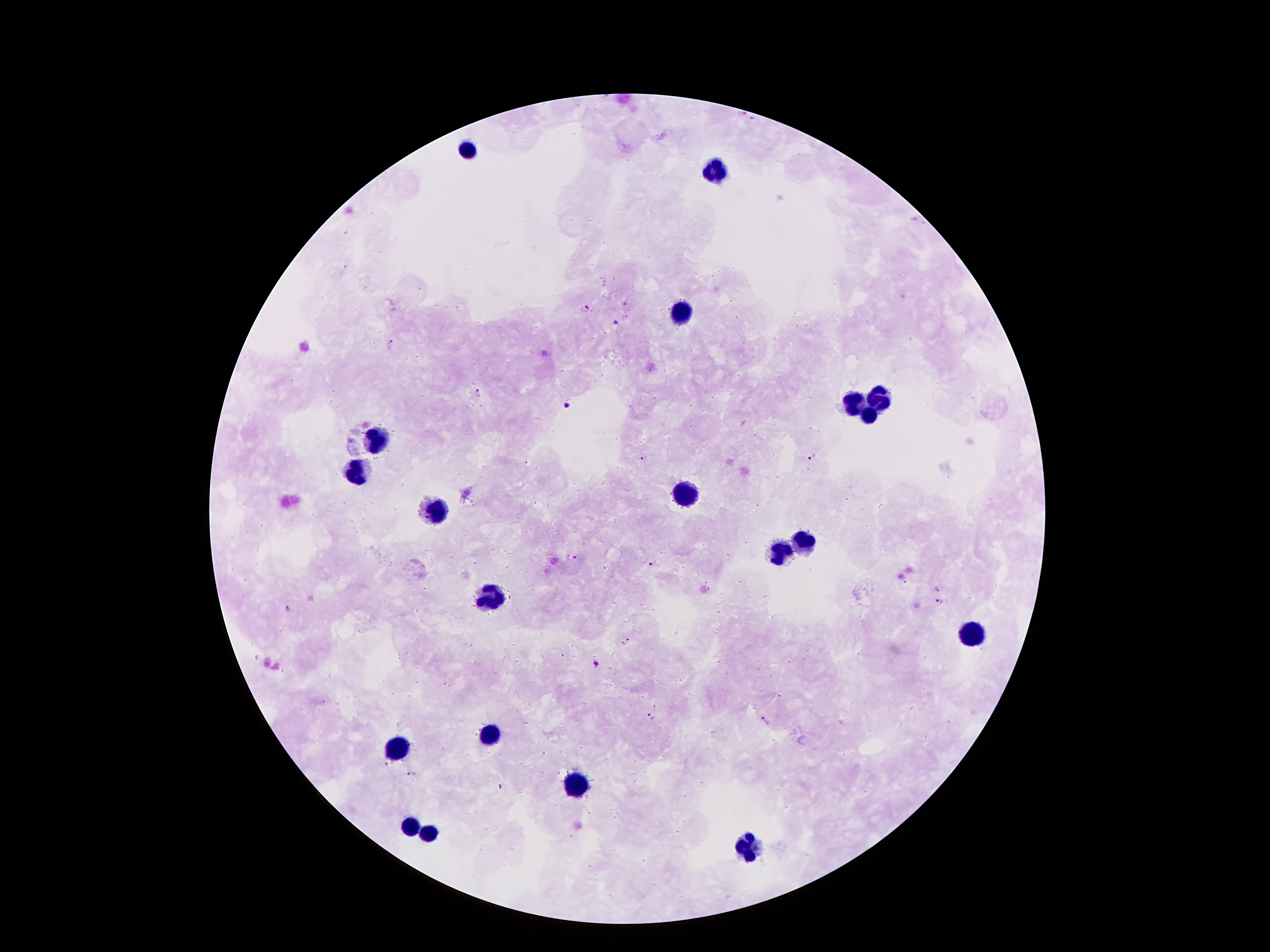
Approximate centers as {x, y} in pixels.
Summary:
  - Leukocyte locations: {469, 149}, {718, 172}, {681, 312}, {878, 396}, {851, 405}, {869, 416}, {380, 439}, {360, 472}, {681, 496}, {435, 511}, {805, 540}, {780, 551}, {495, 597}, {970, 633}, {486, 736}, {393, 746}, {570, 786}, {413, 827}, {429, 833}, {751, 849}
  - Malaria parasite locations: {584, 308}, {615, 321}, {391, 343}, {477, 392}, {567, 404}, {643, 456}, {812, 458}, {571, 557}, {650, 564}, {937, 588}, {940, 601}, {287, 609}, {626, 637}, {595, 665}, {649, 715}, {764, 721}, {383, 763}, {412, 773}, {501, 785}
  - Patient malaria status: infected with Plasmodium falciparum
  - Field of view: one from this slide
  - Image size: 1270×952 pixels
  - Preparation: thick blood film
  - Stain: Giemsa
  - Capture: smartphone camera through the microscope eyepiece
  - Magnification: 100x